Classify this cell by malaria status.
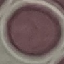

It is uninfected.

capture = smartphone through the microscope eyepiece
image type = cell patch, automatically extracted from a larger field of view and resized to 64 × 64 pixels
preparation = thin blood film
stain = Giemsa